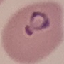

malaria_status: parasitized
stain: Giemsa
image_type: automatically extracted cell patch, resized to 64 × 64 pixels
capture: smartphone camera at the microscope eyepiece
preparation: thin blood film